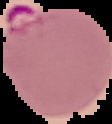

Summary:
  - Image size: 112×124 pixels
  - Result: Plasmodium parasites identified
  - Preparation: thin blood smear
  - Image type: segmented cell region with the area outside set to black